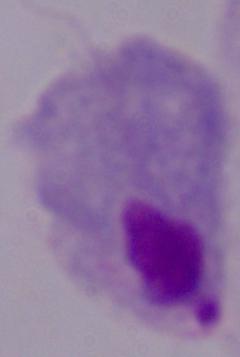

magnification = 1000x
modality = micrograph
identification = trichomonad